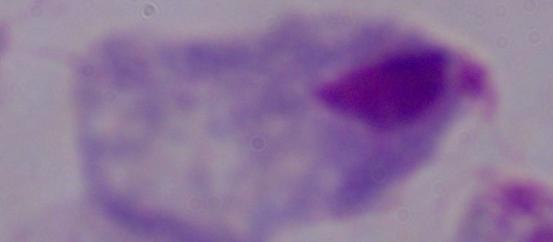
Summary:
  - Magnification: 1000x
  - Modality: photomicrograph
  - Identification: trichomonad